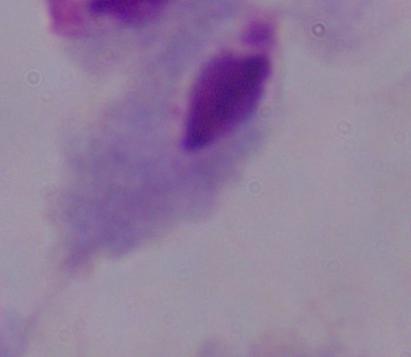 Photomicrograph. A trichomonad is shown. 1000x magnification.